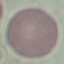
Result: negative for malaria parasites. Giemsa-stained preparation. Acquired by smartphone through the microscope eyepiece. Automatically extracted cell patch, resized to 64 × 64 pixels. Thin blood smear.